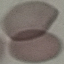
Summary:
  - Result: negative for malaria parasites
  - Preparation: thin smear
  - Image type: automatically extracted cell patch, resized to 64 × 64 pixels
  - Stain: Giemsa
  - Capture: smartphone through the microscope eyepiece